Name the cell type shown.
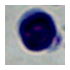

A leukocyte.

Photomicrograph. 1000x magnification.